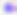
{
  "magnification": "400x",
  "modality": "photomicrograph",
  "identification": "Toxoplasma gondii"
}